State which parasite is depicted.
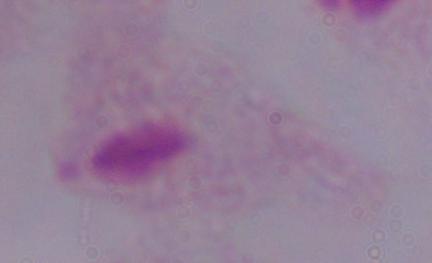
This is a trichomonad.

modality: micrograph
magnification: 1000x